Give the extent of all Plasmodium malariae-infected red blood cells.
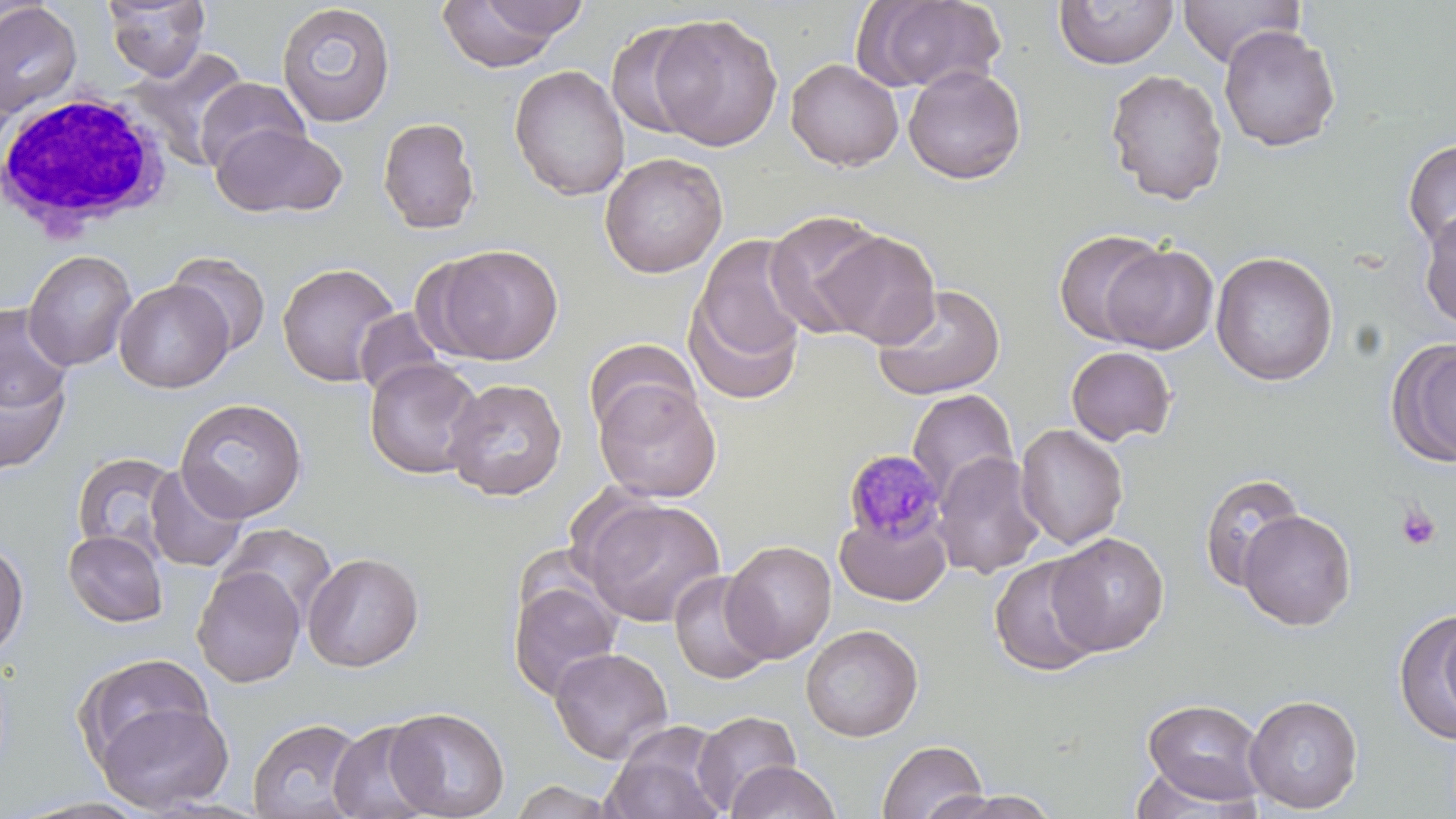

Approximate bounding boxes as (x1,y1)-(x2,y2) corner pairs in pixels.
Plasmodium malariae-infected red blood cells: (843,450)-(948,546).

White blood cell locations: (3,89)-(175,242). Uninfected red blood cell locations: (103,0)-(210,81), (435,0)-(574,71), (856,0)-(1006,94), (1177,0)-(1305,68), (1053,1)-(1178,70), (0,2)-(82,117), (471,2)-(592,42), (276,3)-(395,127), (649,13)-(784,151), (605,20)-(712,142), (1219,25)-(1341,152), (127,48)-(251,171), (785,58)-(904,171), (509,64)-(631,201), (903,64)-(1026,184), (1104,68)-(1228,205), (196,78)-(309,174), (377,117)-(481,234), (211,123)-(346,219), (1402,139)-(1456,254), (599,152)-(728,278), (1418,209)-(1456,331), (764,211)-(889,339), (813,227)-(939,348), (1053,228)-(1169,345), (686,234)-(811,398), (1098,243)-(1220,355), (427,244)-(563,365), (22,249)-(137,372), (168,251)-(271,358), (1210,251)-(1339,386), (277,262)-(400,387), (114,279)-(234,393), (871,283)-(1006,400), (1,303)-(73,414), (353,307)-(447,400), (584,338)-(700,440), (1387,338)-(1456,467), (1065,346)-(1177,446), (364,358)-(485,480), (0,365)-(70,475), (443,378)-(568,501), (594,381)-(721,503), (905,389)-(1019,505), (174,397)-(308,522), (1014,423)-(1128,549), (71,451)-(183,561), (932,451)-(1046,579), (144,465)-(249,573), (1198,471)-(1305,592), (580,496)-(726,628), (1238,510)-(1357,631), (835,512)-(951,606), (218,522)-(337,623), (63,529)-(169,628), (1046,532)-(1169,656), (0,540)-(29,658), (721,540)-(837,663), (302,551)-(425,671), (989,555)-(1104,677), (192,565)-(306,687), (669,570)-(774,685), (508,579)-(622,701), (1396,609)-(1456,744), (1437,610)-(1456,737), (800,624)-(923,742), (550,646)-(674,764), (73,654)-(214,768), (1244,695)-(1363,813), (1142,697)-(1266,805), (95,700)-(234,814), (384,707)-(511,819), (691,710)-(802,814), (247,717)-(367,819), (327,719)-(439,819), (602,723)-(730,819), (877,739)-(987,819), (724,760)-(841,819), (1128,766)-(1258,817), (508,779)-(622,819), (926,790)-(1062,819). Platelet locations: (1396,504)-(1442,551). Slide-level diagnosis: Plasmodium malariae. Single field of view. Light microscopy. May-Grünwald-Giemsa stain. Thin blood film. Captured at 1000x magnification. Image is 1456×819 pixels.